Locate every malaria parasite by life-cycle stage, and every leukocyte.
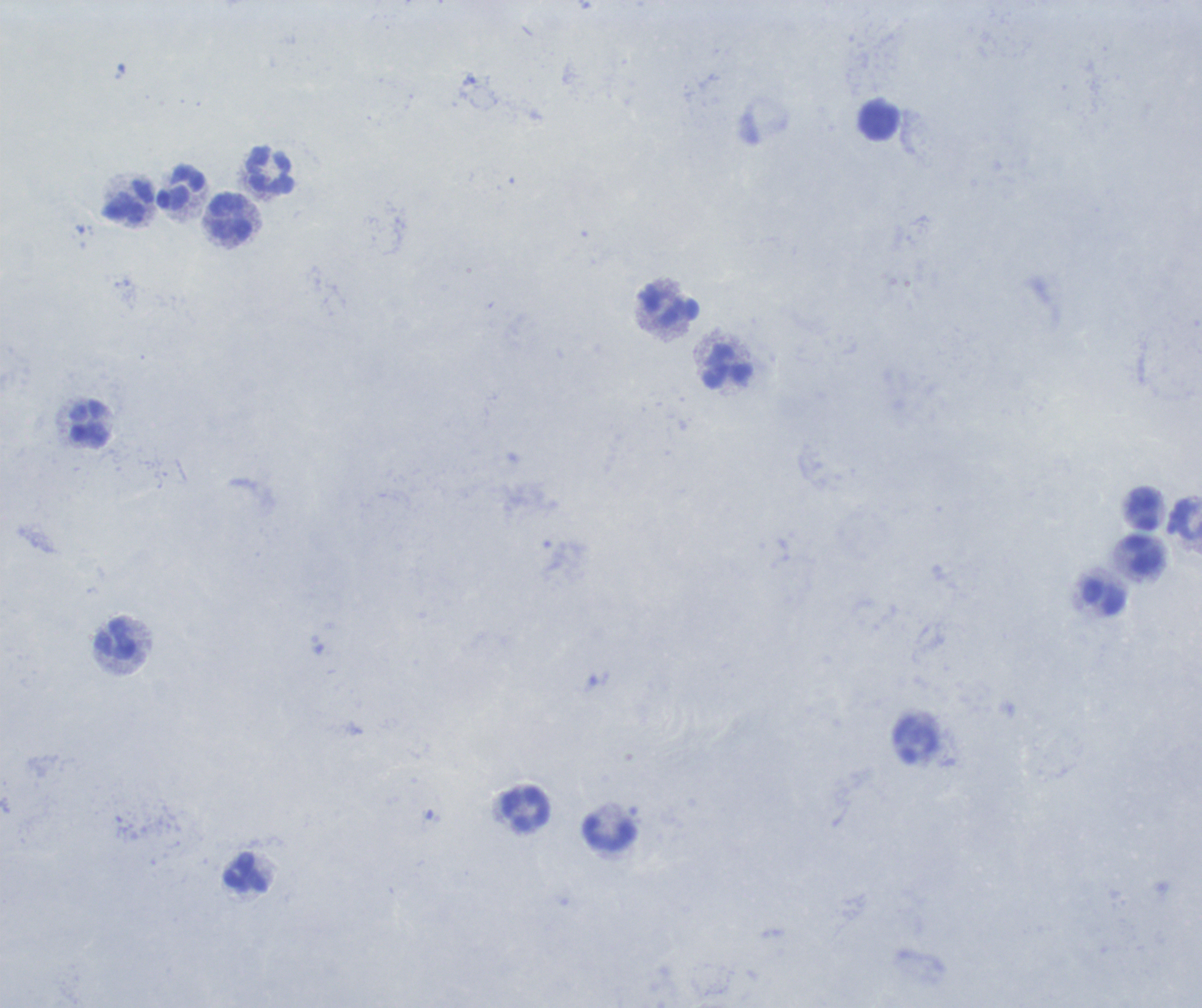
No malaria parasites seen.
Approximate centers as {x, y} in pixels.
Leukocytes: {879, 121}, {271, 171}, {181, 189}, {127, 203}, {230, 216}, {670, 305}, {727, 368}, {90, 425}, {1143, 509}, {1185, 520}, {1144, 555}, {1104, 596}, {116, 640}, {525, 807}, {609, 833}, {246, 873}.

Summary:
  - Field of view: single
  - Preparation: thick blood smear
  - Image size: 1202×1008 pixels
  - Context: previously used in a real diagnosis
  - Magnification: 100x
  - Stain: Romanowsky
  - Background quality: unsatisfactory